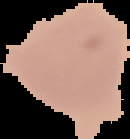
Summary:
  - Image type: cell region segmented out of the field of view; surrounding area masked to black
  - Preparation: thin blood film
  - Image size: 130×139 pixels
  - Result: no Plasmodium parasites detected